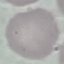
Summary:
  - Result: no malaria parasites seen
  - Stain: Giemsa
  - Image type: automatically extracted cell patch, resized to 64 × 64 pixels
  - Preparation: thin smear
  - Capture: smartphone camera at the microscope eyepiece